Give the position of every leukocyte visible.
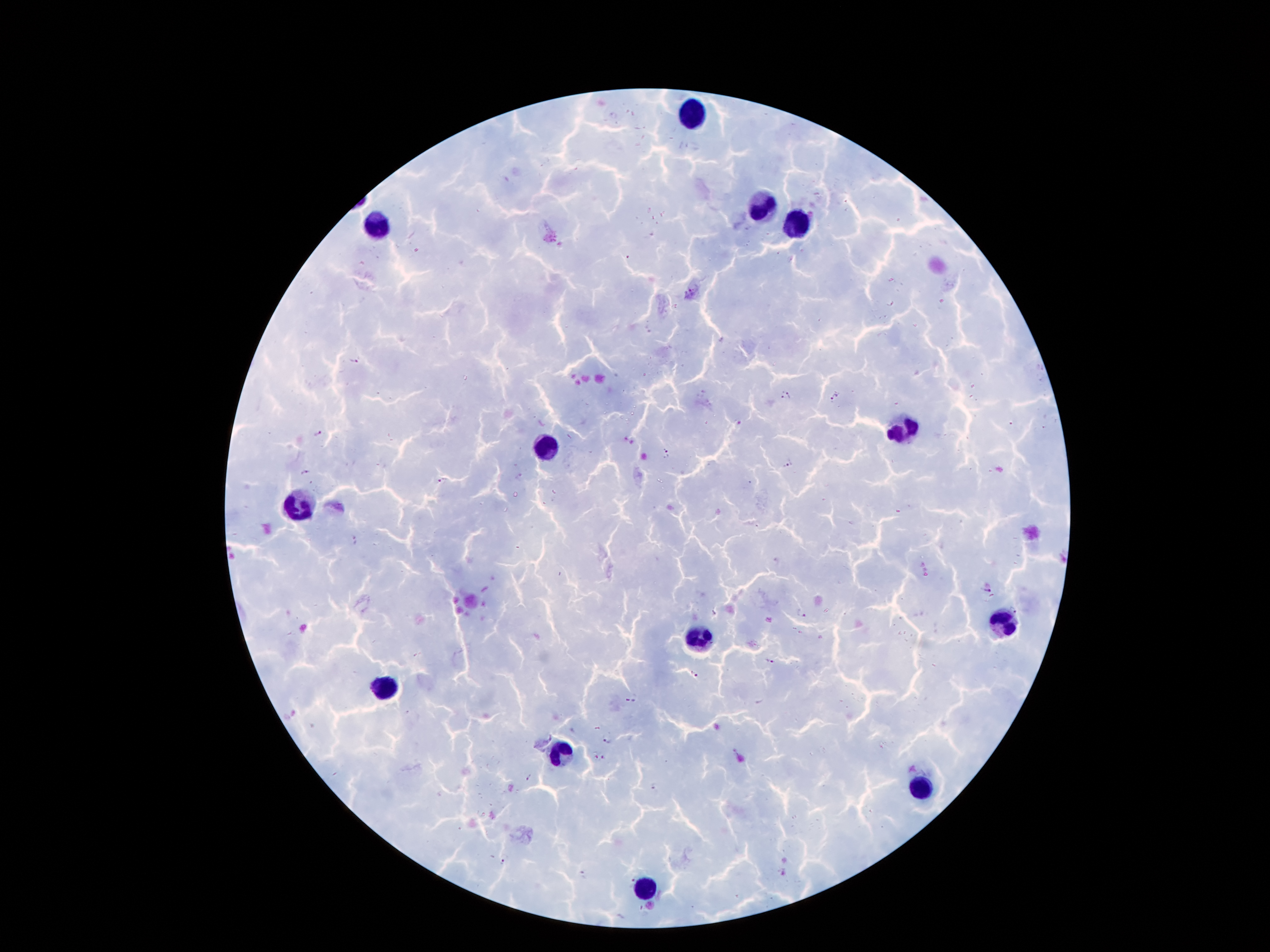
Approximate object centers, in pixels from the top-left corner.
Leukocytes: (x=698, y=114), (x=761, y=203), (x=378, y=223), (x=793, y=228), (x=902, y=427), (x=543, y=445), (x=298, y=504), (x=1002, y=625), (x=695, y=634), (x=382, y=688), (x=559, y=752), (x=922, y=786), (x=646, y=890).

Plasmodium parasite locations = (x=355, y=360), (x=785, y=394), (x=835, y=396), (x=316, y=433), (x=666, y=452), (x=789, y=464), (x=306, y=474), (x=520, y=477), (x=443, y=481), (x=355, y=542), (x=985, y=591), (x=802, y=613), (x=768, y=662), (x=694, y=673), (x=630, y=700), (x=607, y=739), (x=595, y=755), (x=605, y=757), (x=528, y=778), (x=655, y=787), (x=503, y=863), (x=784, y=872), (x=584, y=876), (x=627, y=880)
patient malaria status = infected with Plasmodium falciparum
preparation = thick blood film
image size = 1270×952 pixels
capture = smartphone through the microscope eyepiece
magnification = 100x
stain = Giemsa
field of view = single